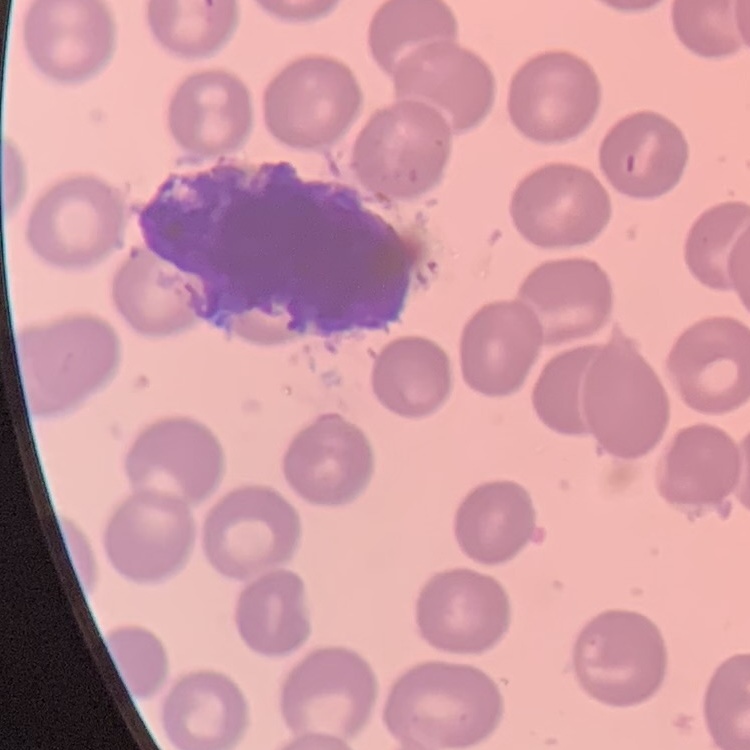

The red blood cells show no rouleaux formation. Thin peripheral smear. Field's or Giemsa stain. Square crop of a larger photomicrograph.